Locate every blood parasite and identify its species.
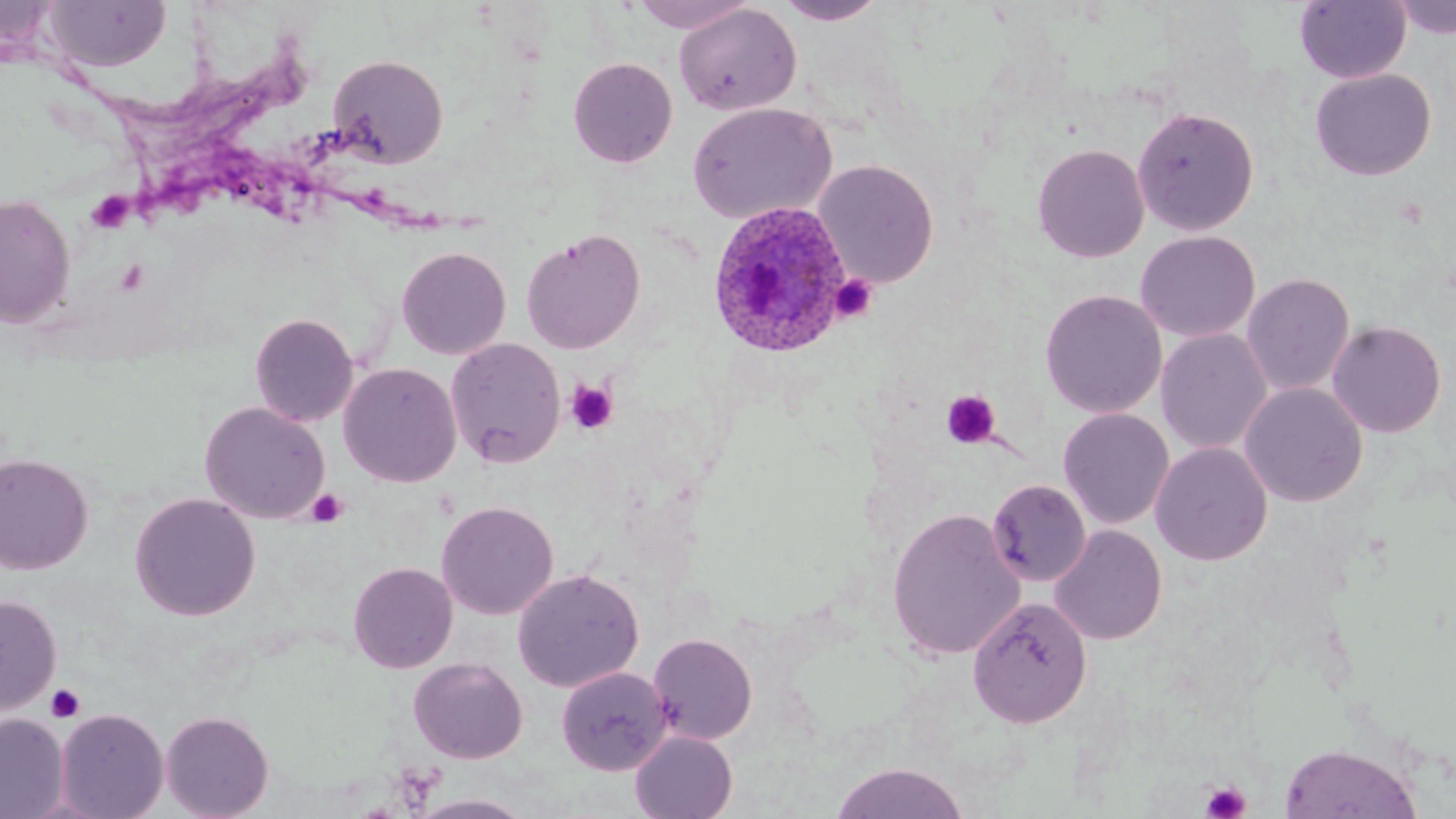
Approximate bounding boxes as (x1,y1)-(x2,y2) corner pairs in pixels.
Plasmodium ovale-infected red blood cells (subset): (706,201)-(854,359).
No Plasmodium falciparum, Plasmodium malariae, Plasmodium vivax, Babesia divergens, or Trypanosoma brucei observed.

Summary:
  - Uninfected red blood cell locations (subset): (627,0)-(757,33), (1389,0)-(1456,41), (43,1)-(172,72), (774,1)-(888,25), (1294,1)-(1411,84), (674,3)-(801,117), (328,54)-(449,168), (568,57)-(678,168), (1309,68)-(1437,181), (687,101)-(837,225), (1132,105)-(1260,236), (1031,143)-(1150,263), (814,159)-(939,288), (0,193)-(76,329), (521,227)-(646,355), (1135,230)-(1260,343), (396,245)-(512,360), (1241,272)-(1355,396), (1039,289)-(1167,419), (250,313)-(359,427), (1326,320)-(1447,438), (1155,328)-(1273,455), (446,337)-(566,469), (338,362)-(462,488), (1240,382)-(1368,507), (199,402)-(329,524), (1058,408)-(1175,530), (1151,442)-(1273,566), (0,453)-(94,574), (129,492)-(261,621), (436,500)-(559,620), (886,507)-(1027,660), (1049,524)-(1167,645), (348,561)-(458,673), (512,568)-(645,692), (0,595)-(61,716), (967,595)-(1093,729), (648,633)-(758,744), (408,657)-(528,764), (556,666)-(671,775), (55,709)-(169,818), (160,710)-(274,819), (0,713)-(69,818), (629,731)-(738,818), (1279,743)-(1423,818), (831,760)-(970,819), (406,793)-(536,818)
  - Platelet locations: (86,191)-(134,235), (829,274)-(878,323), (565,380)-(618,435), (941,389)-(1001,449), (307,489)-(348,528), (46,683)-(86,723), (1201,781)-(1251,819)
  - Slide-level diagnosis: Plasmodium ovale
  - Magnification: 1000x
  - Field of view: single
  - Image size: 1456×819 pixels
  - Preparation: thin blood smear
  - Modality: light microscopy
  - Stain: May-Grünwald-Giemsa